Name the parasite shown.
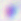
This is Toxoplasma gondii.

Summary:
  - Modality: micrograph
  - Magnification: 400x